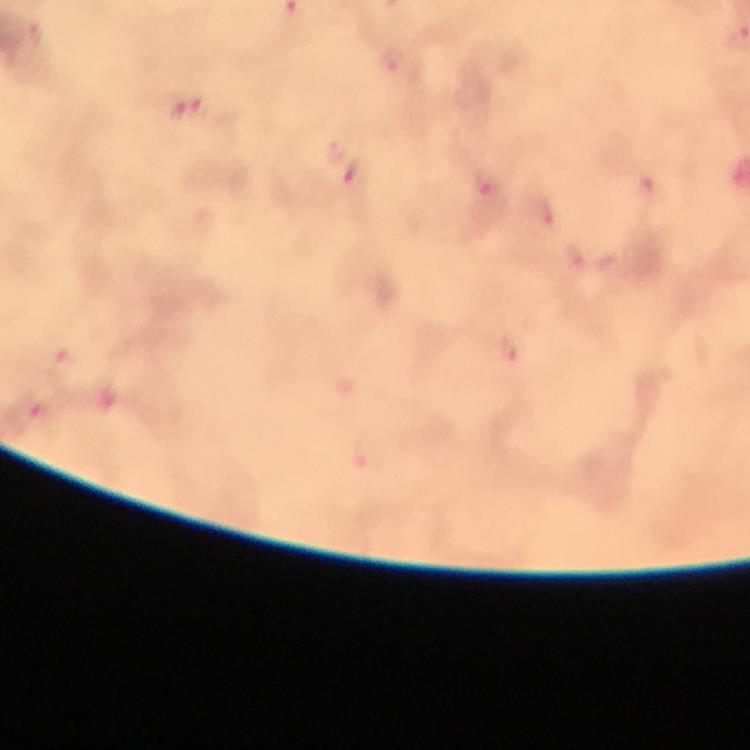

{
  "context": "from a malaria diagnostic workup",
  "preparation": "thick blood smear",
  "capture": "smartphone camera through the microscope",
  "immersion_oil": "used",
  "magnification": "100x",
  "malaria_parasite_locations": "approximate object centers, in pixels from the top-left corner: (x=33, y=38), (x=392, y=62), (x=188, y=109), (x=354, y=176), (x=544, y=212), (x=507, y=349), (x=27, y=412)",
  "cropped_from": "a single field of view",
  "image_size": "750×750 pixels",
  "stain": "Giemsa"
}